Outline each blood parasite and name the species.
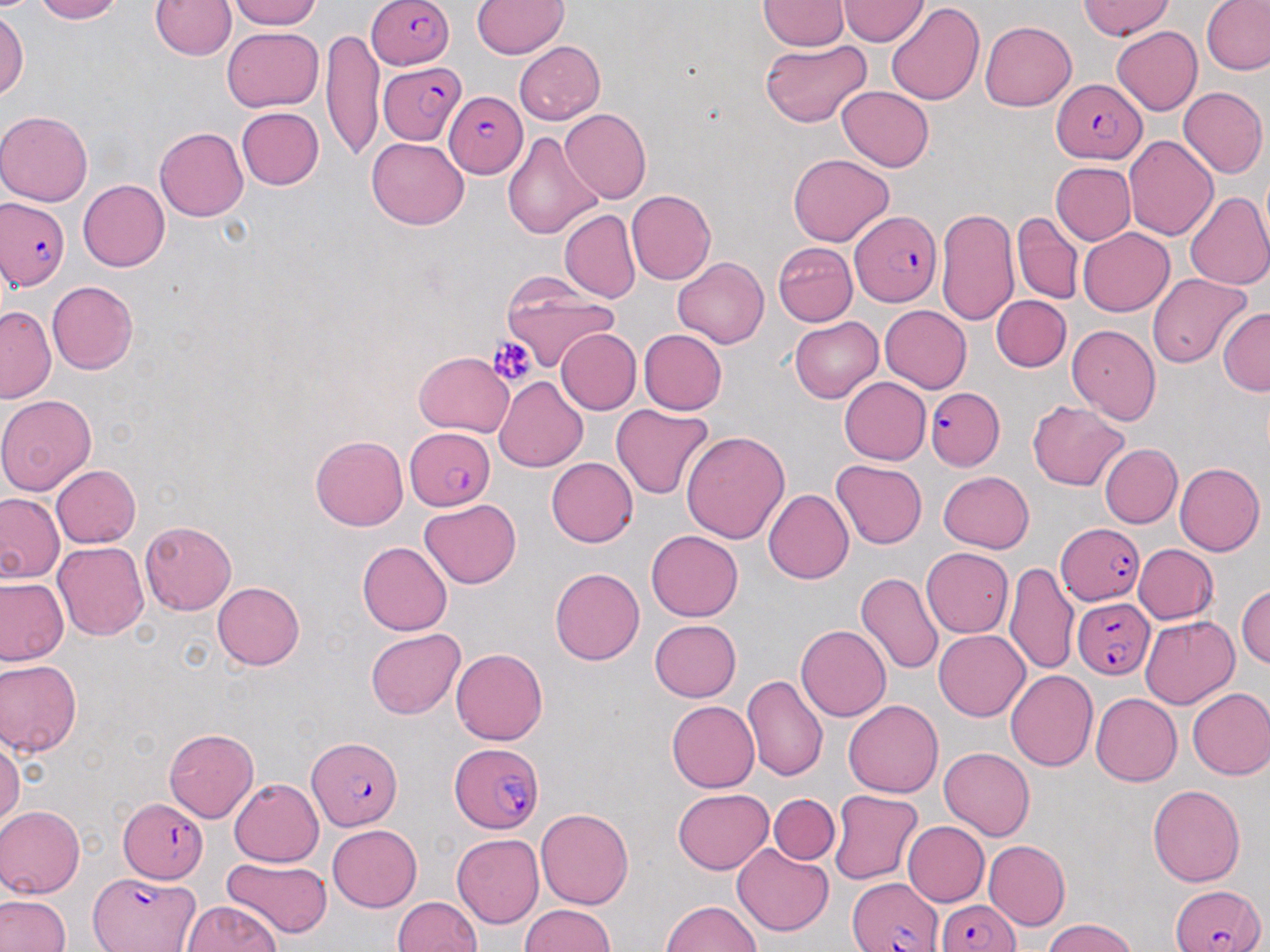

Approximate bounding boxes as (x1, y1, x2, y2) in pixels.
Plasmodium falciparum-infected red blood cells: (367, 0, 450, 69), (380, 62, 466, 144), (1052, 81, 1147, 162), (446, 90, 528, 176), (3, 198, 70, 288), (850, 210, 941, 306), (925, 387, 1005, 469), (405, 427, 496, 511), (1057, 524, 1146, 607), (1074, 594, 1153, 678), (306, 736, 404, 831), (447, 743, 546, 831), (117, 797, 210, 883), (89, 871, 203, 951), (849, 877, 945, 952), (1170, 882, 1264, 952), (935, 892, 1021, 952).
No Plasmodium ovale, Plasmodium malariae, Plasmodium vivax, Babesia divergens, or Trypanosoma brucei observed.

Uninfected red blood cell locations: (28, 0, 123, 24), (226, 0, 329, 29), (472, 0, 569, 59), (759, 0, 846, 51), (1202, 0, 1270, 77), (151, 1, 234, 60), (839, 1, 926, 45), (886, 1, 986, 106), (1077, 1, 1180, 40), (0, 7, 27, 109), (980, 21, 1076, 110), (1112, 25, 1203, 115), (224, 26, 323, 110), (324, 33, 382, 160), (759, 41, 871, 127), (513, 42, 607, 124), (836, 85, 933, 171), (1179, 85, 1268, 178), (236, 107, 323, 190), (562, 109, 651, 202), (0, 112, 94, 207), (153, 127, 247, 221), (503, 128, 600, 244), (1123, 135, 1217, 242), (368, 137, 467, 229), (786, 154, 894, 245), (1049, 163, 1135, 245), (78, 179, 170, 271), (627, 189, 717, 283), (1186, 189, 1270, 288), (936, 207, 1021, 329), (559, 211, 640, 303), (1012, 213, 1084, 304), (1078, 229, 1175, 315), (773, 241, 859, 326), (673, 257, 768, 348), (499, 269, 623, 370), (1148, 272, 1253, 367), (46, 279, 139, 374), (992, 296, 1070, 372), (1, 303, 57, 405), (880, 306, 970, 393), (1218, 307, 1270, 394), (789, 317, 883, 402), (1068, 323, 1162, 424), (640, 328, 727, 415), (555, 330, 640, 415), (415, 354, 513, 436), (494, 376, 590, 471), (837, 376, 931, 464), (0, 393, 98, 496), (1026, 398, 1133, 491), (612, 403, 713, 500), (683, 429, 788, 548), (309, 434, 408, 531), (1098, 444, 1181, 528), (547, 457, 637, 548), (833, 461, 926, 549), (1175, 463, 1264, 555), (51, 464, 143, 548), (937, 471, 1037, 553), (763, 488, 853, 584), (0, 494, 64, 585), (420, 499, 522, 587), (138, 522, 237, 615), (647, 530, 743, 620), (53, 541, 148, 643), (357, 541, 451, 635), (1134, 543, 1217, 624), (923, 546, 1014, 637), (1007, 561, 1079, 676), (549, 567, 644, 666), (855, 572, 943, 677), (1, 577, 67, 666), (213, 580, 305, 670), (1239, 583, 1270, 672), (1140, 615, 1239, 706), (649, 619, 742, 702), (797, 623, 893, 721), (366, 628, 464, 719), (933, 630, 1032, 721), (452, 647, 548, 745), (0, 659, 80, 759), (1006, 670, 1098, 772), (742, 675, 828, 784), (1187, 688, 1270, 780), (1089, 692, 1182, 786), (844, 700, 943, 797), (666, 701, 759, 792), (164, 728, 259, 822), (0, 738, 23, 832), (939, 747, 1036, 839), (229, 776, 324, 864), (1148, 783, 1246, 888), (673, 789, 773, 873), (829, 790, 922, 884), (770, 793, 838, 864), (0, 806, 82, 899), (536, 809, 633, 908), (901, 820, 989, 907), (326, 824, 422, 911), (454, 834, 544, 928), (982, 841, 1069, 930), (733, 846, 834, 936), (221, 860, 328, 938), (1, 893, 70, 952), (392, 896, 481, 952), (659, 899, 765, 952), (179, 900, 282, 952), (517, 905, 616, 952), (1038, 920, 1142, 952). Platelet locations: (489, 335, 536, 388). Slide-level diagnosis: Plasmodium falciparum. 1000x magnification. Image is 1270×952 pixels. Optical microscopy. May-Grünwald-Giemsa stain. Thin blood film. One field of a larger specimen.